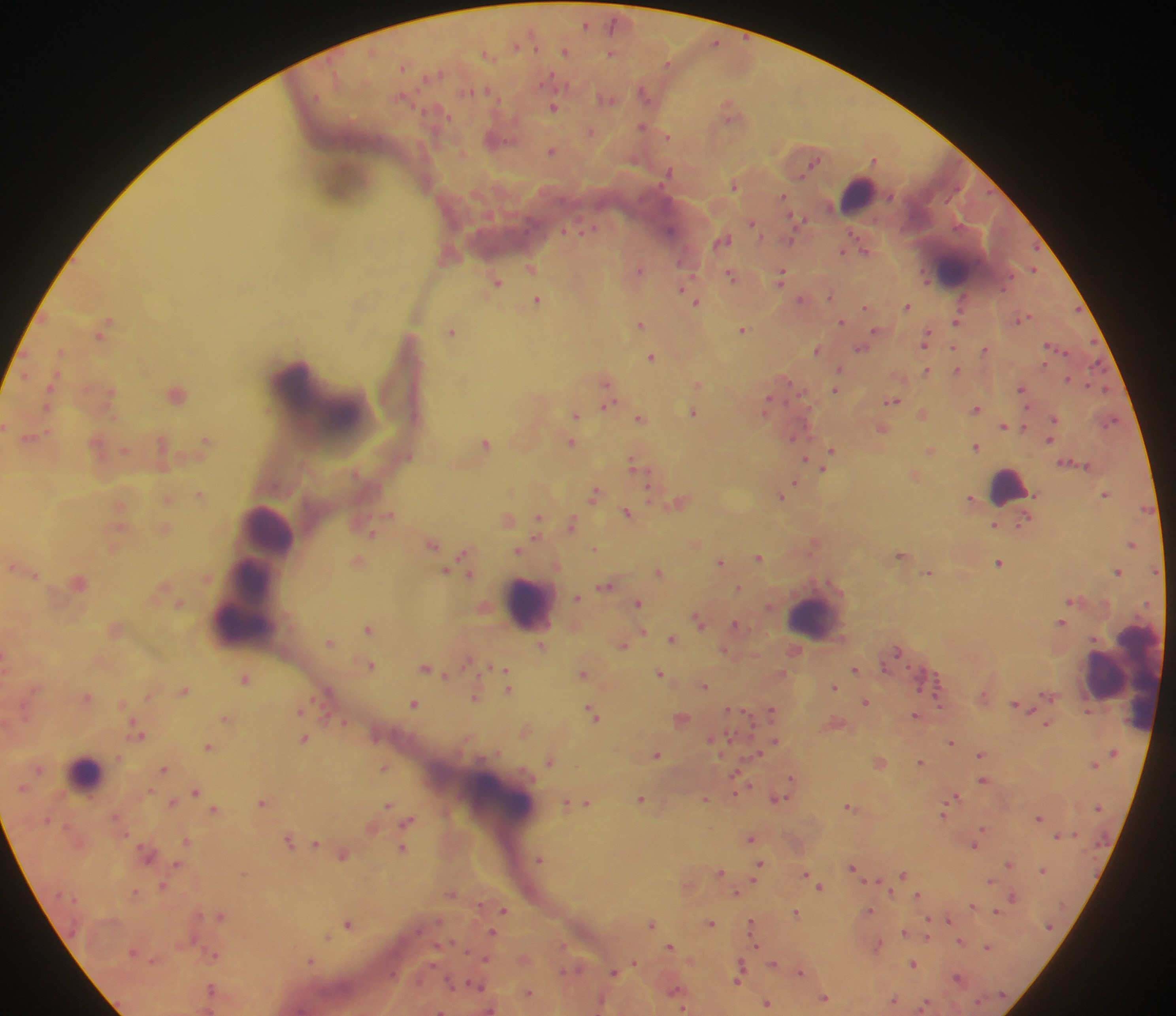

Approximate centers as [x, y] in pixels. Malaria parasite locations: [586, 23], [715, 42], [566, 50], [611, 52], [488, 54], [669, 63], [436, 73], [551, 76], [645, 92], [608, 96], [554, 106], [731, 109], [642, 125], [590, 130], [667, 134], [497, 137], [553, 150], [462, 152], [875, 158], [812, 163], [670, 171], [734, 184], [783, 196], [800, 218], [751, 220], [670, 230], [723, 237], [790, 238], [865, 248], [843, 250], [449, 253], [531, 266], [639, 268], [1033, 268], [732, 274], [781, 274], [926, 275], [497, 279], [682, 290], [830, 295], [690, 296], [802, 298], [538, 299], [696, 300], [908, 305], [866, 306], [1023, 317], [957, 318], [842, 320], [641, 322], [104, 326], [743, 328], [452, 329], [879, 330], [926, 338], [954, 345], [861, 347], [817, 348], [986, 348], [60, 351], [651, 356], [840, 367], [956, 368], [926, 369], [1068, 378], [607, 379], [698, 383], [1022, 388], [835, 389], [110, 391], [177, 391], [893, 400], [767, 402], [48, 403], [606, 404], [976, 407], [693, 410], [576, 412], [922, 412], [641, 417], [1055, 418], [1110, 419], [1005, 424], [1024, 424], [6, 425], [882, 427], [31, 436], [1050, 437], [205, 440], [571, 441], [485, 442], [98, 443], [162, 443], [976, 445], [931, 449], [125, 450], [832, 450], [805, 458], [636, 463], [824, 467], [914, 474], [795, 480], [650, 487], [595, 492], [1106, 492], [200, 493], [781, 495], [167, 497], [971, 497], [679, 502], [121, 506], [628, 512], [390, 513], [508, 517], [539, 518], [1024, 521], [572, 523], [994, 523], [165, 527], [373, 532], [695, 541], [1132, 542], [432, 543], [815, 543], [113, 547], [594, 547], [520, 549], [466, 553], [902, 553], [759, 556], [357, 559], [721, 561], [1000, 561], [13, 565], [1156, 569], [445, 570], [659, 570], [1118, 570], [469, 571], [928, 572], [34, 573], [78, 579], [606, 585], [738, 586], [577, 596], [179, 602], [638, 602], [699, 618], [1061, 621], [735, 624], [369, 627], [115, 629], [643, 630], [671, 637], [329, 641], [624, 644], [541, 645], [726, 649], [468, 660], [370, 663], [427, 666], [855, 668], [505, 671], [583, 671], [660, 673], [247, 677], [704, 684], [508, 685], [834, 686], [185, 688], [327, 692], [1050, 693], [149, 694], [88, 695], [475, 696], [866, 700], [122, 702], [414, 703], [1018, 704], [301, 708], [732, 708], [772, 709], [593, 711], [917, 714], [226, 717], [681, 717], [344, 721], [837, 723], [1048, 723], [526, 728], [137, 731], [713, 737], [305, 738], [775, 739], [951, 741], [209, 745], [657, 753], [759, 753], [982, 753], [550, 758], [880, 760], [921, 761], [1095, 762], [385, 766], [164, 767], [737, 772], [792, 778], [984, 779], [197, 789], [735, 791], [195, 793], [955, 794], [641, 797], [705, 797], [777, 797], [173, 801], [263, 801], [567, 801], [583, 802], [389, 803], [850, 805], [215, 809], [944, 811], [1039, 817], [408, 820], [371, 826], [983, 828], [1058, 835], [751, 837], [289, 839], [186, 840], [977, 840], [316, 841], [975, 844], [403, 847], [343, 852], [540, 857], [1009, 862], [177, 863], [759, 864], [853, 866], [1043, 869], [721, 871], [244, 872], [805, 872], [904, 872], [877, 879], [991, 879], [162, 884], [688, 884], [820, 885], [891, 889], [136, 891], [451, 892], [737, 892], [918, 894], [1013, 896], [973, 904], [504, 909], [870, 909], [997, 910], [796, 911], [221, 915], [948, 918], [652, 921], [349, 922], [711, 922], [752, 924], [906, 931], [493, 932], [928, 935], [329, 936], [960, 939], [877, 945], [670, 946], [989, 946], [214, 953], [524, 957], [487, 958], [691, 959], [311, 960], [635, 962], [773, 962], [913, 962], [572, 969], [741, 971], [800, 971], [614, 972], [959, 976], [478, 984], [211, 989], [529, 992], [677, 992], [824, 997], [894, 1000], [766, 1002], [489, 1008], [683, 1008], [440, 1010]. Leukocyte locations: [345, 180], [858, 193], [952, 269], [1008, 485], [267, 529], [249, 599], [528, 603], [815, 614], [1109, 675], [1123, 678], [85, 772], [497, 799]. Collected in Ghana. Image is 1176×1016 pixels. Thick blood smear. Photographed through a microscope with a mobile-phone camera. One field of view.